State the preparation type.
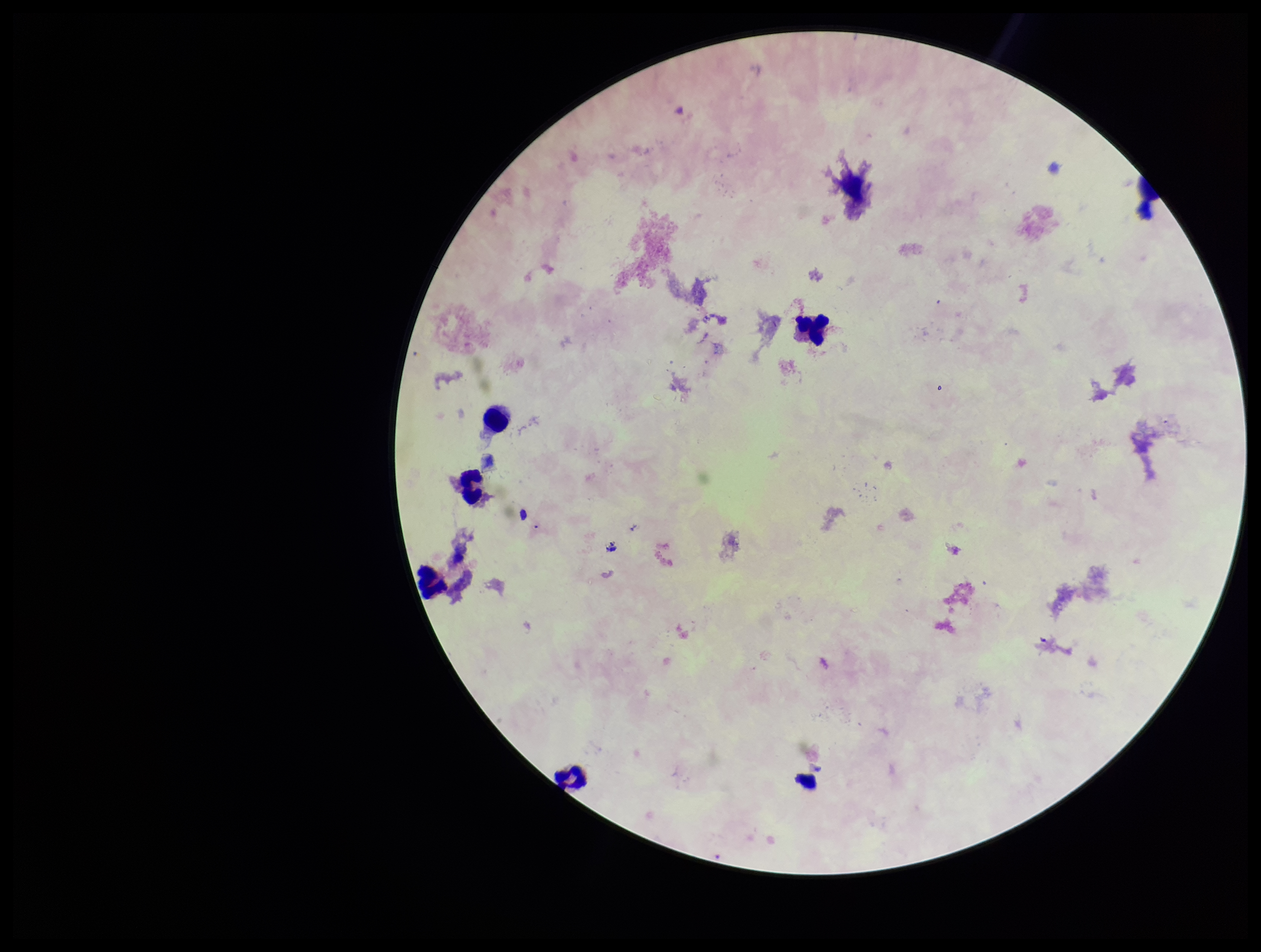
Thick.

Single field of view. Giemsa stain. Patient malaria status: infected. Parasite count: 0. Plasmodium parasites: none seen. Image is 1261×952 pixels. Leukocyte count: 7. Smartphone photograph taken through the eyepiece of a microscope. Species reported for this patient: Plasmodium falciparum.